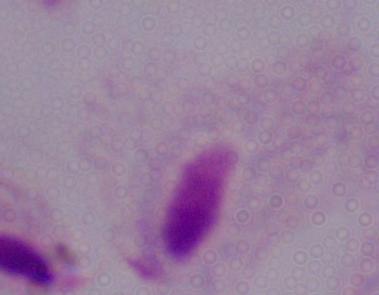
modality = photomicrograph
magnification = 1000x
identification = trichomonad